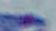

{
  "modality": "micrograph",
  "magnification": "1000x",
  "identification": "Toxoplasma gondii"
}